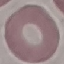

Result: no malaria parasites seen. Thin blood smear. Cell patch, automatically extracted from a larger field of view and resized to 64 × 64 pixels. Photographed with a smartphone camera at the microscope eyepiece. Giemsa-stained preparation.